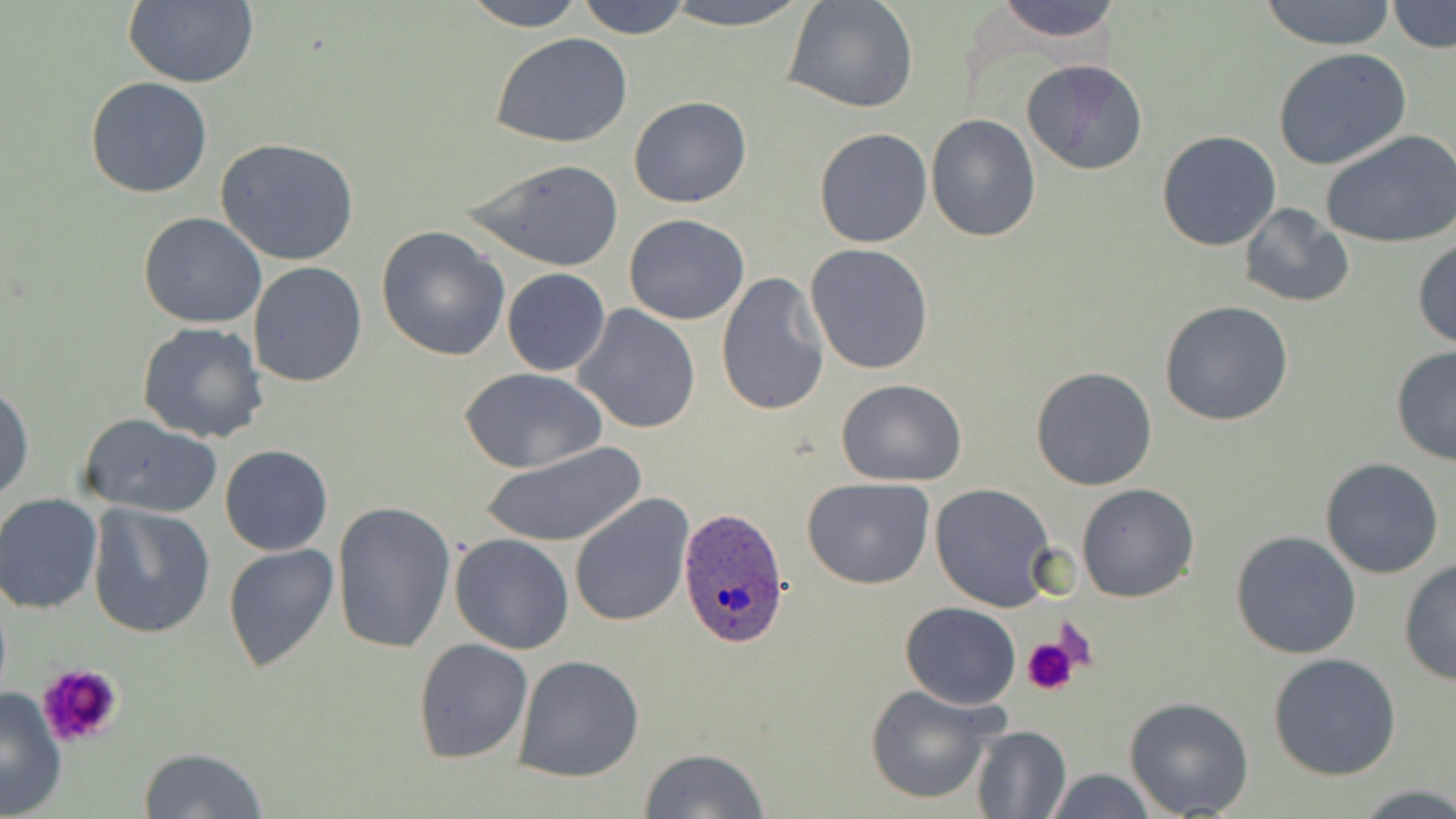

Approximate bounding boxes as (x1, y1, x2, y2) in pixels. Platelet locations: (1052, 621, 1101, 676), (1023, 636, 1080, 696), (34, 662, 126, 750). Plasmodium ovale-infected red blood cell locations: (676, 506, 791, 648). Uninfected red blood cell locations: (123, 0, 259, 88), (460, 0, 587, 31), (575, 0, 693, 41), (656, 0, 811, 31), (988, 0, 1129, 48), (1259, 0, 1398, 50), (784, 1, 917, 113), (1388, 2, 1453, 53), (493, 33, 633, 149), (1273, 49, 1413, 172), (1021, 59, 1149, 174), (83, 76, 213, 199), (627, 96, 751, 207), (926, 113, 1041, 243), (812, 128, 932, 248), (1320, 129, 1456, 249), (1157, 130, 1281, 251), (216, 138, 361, 266), (462, 156, 626, 273), (1238, 201, 1356, 309), (138, 212, 267, 328), (623, 212, 750, 324), (376, 225, 511, 359), (1412, 237, 1456, 349), (804, 243, 933, 375), (248, 261, 367, 387), (502, 269, 611, 376), (716, 272, 829, 416), (1160, 299, 1295, 427), (572, 303, 702, 433), (138, 320, 269, 442), (1390, 345, 1456, 467), (1030, 366, 1158, 490), (461, 368, 606, 472), (0, 378, 34, 503), (836, 380, 967, 487), (77, 412, 225, 518), (479, 440, 647, 549), (220, 445, 332, 557), (1320, 456, 1445, 579), (802, 477, 934, 588), (929, 481, 1057, 610), (1077, 483, 1199, 602), (570, 492, 693, 627), (0, 494, 103, 614), (88, 502, 217, 638), (332, 503, 457, 653), (1230, 530, 1361, 660), (450, 532, 575, 654), (223, 544, 342, 673), (1398, 558, 1455, 685), (900, 602, 1020, 709), (413, 637, 533, 764), (1267, 652, 1401, 780), (513, 654, 644, 781), (864, 683, 1000, 805), (0, 687, 69, 819), (1124, 697, 1254, 818), (968, 724, 1072, 818), (138, 746, 270, 819), (639, 748, 768, 819), (1040, 767, 1158, 819), (1359, 785, 1456, 818). Slide-level diagnosis: Plasmodium ovale. Single field of view. Optical microscopy. Image is 1456×819 pixels. May-Grünwald-Giemsa-stained preparation. Thin blood film. Captured at 1000x magnification.